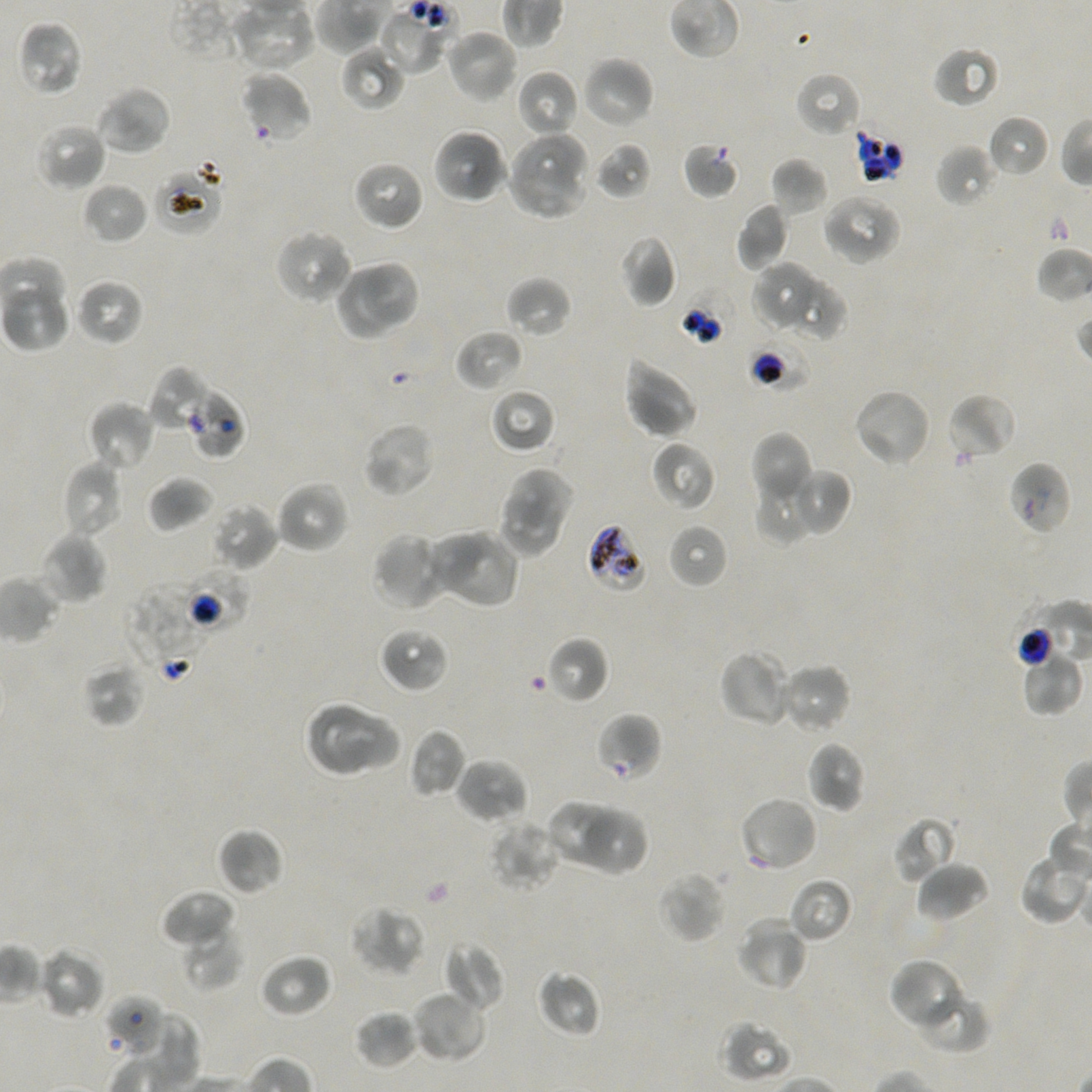 Approximate bounding boxes as (x1, y1, x2, y2) in pixels. Not every red blood cell is marked. Locations of uninfected red blood cells: (378, 9, 446, 75), (18, 20, 84, 98), (444, 28, 519, 104), (932, 44, 1001, 108), (340, 46, 404, 112), (581, 56, 655, 130), (515, 69, 579, 140), (795, 71, 862, 138), (93, 85, 172, 156), (986, 114, 1051, 179), (34, 121, 107, 192), (509, 124, 589, 194), (433, 128, 508, 205), (594, 141, 653, 200), (936, 144, 999, 208), (770, 157, 828, 217), (352, 160, 424, 232), (505, 166, 592, 221), (82, 181, 148, 244), (821, 192, 903, 266), (735, 202, 790, 270), (273, 228, 354, 306), (619, 234, 677, 307), (361, 259, 421, 329), (752, 261, 822, 331), (331, 267, 400, 342), (505, 276, 572, 338), (784, 276, 847, 341), (75, 278, 145, 346), (454, 329, 525, 392), (622, 354, 699, 440), (490, 387, 556, 454), (852, 388, 932, 469), (946, 393, 1017, 462), (88, 401, 157, 472), (361, 421, 436, 499), (751, 430, 813, 511), (651, 441, 716, 511), (60, 460, 124, 537), (502, 466, 575, 528), (755, 466, 819, 545), (787, 467, 852, 536), (147, 475, 215, 532), (274, 480, 350, 555), (496, 492, 562, 564), (210, 503, 278, 572), (667, 523, 728, 589), (444, 530, 520, 610), (424, 531, 488, 594), (39, 532, 108, 606), (372, 532, 447, 612), (378, 626, 450, 693), (545, 636, 611, 705), (1019, 647, 1083, 716), (719, 649, 795, 727), (81, 659, 147, 728), (777, 663, 852, 735), (304, 700, 376, 777), (333, 711, 403, 774), (409, 727, 467, 798), (806, 741, 867, 814), (454, 757, 528, 824), (737, 795, 819, 874), (546, 800, 621, 865), (582, 810, 647, 875), (892, 816, 958, 884), (488, 817, 562, 892), (217, 827, 284, 896), (1019, 852, 1091, 924), (913, 860, 989, 922), (657, 870, 727, 944), (788, 877, 853, 944), (160, 888, 236, 949), (349, 905, 426, 977), (735, 917, 808, 992), (181, 923, 243, 991), (444, 941, 505, 1013), (37, 947, 106, 1019), (259, 953, 333, 1018), (888, 956, 968, 1031), (535, 968, 602, 1038), (907, 982, 991, 1054), (410, 990, 487, 1063), (354, 1008, 418, 1069), (130, 1011, 200, 1089), (718, 1017, 793, 1082). Locations of red blood cells of indeterminate infection status: (240, 71, 312, 141), (854, 129, 903, 183), (683, 141, 740, 199), (153, 164, 224, 236), (746, 333, 812, 392), (148, 367, 211, 434), (185, 385, 246, 460), (1008, 460, 1072, 536), (587, 522, 649, 593), (181, 566, 250, 636), (124, 584, 216, 682), (1014, 600, 1066, 675), (596, 712, 661, 782), (105, 993, 168, 1057). P. falciparum strain NF54 maintained in static in-vitro culture. Giemsa-stained preparation. Thin blood film. Image is 1092×1092 pixels. One field from this slide. Oil immersion, 100x objective (numerical aperture 1.45). Donor blood group A+/O+.